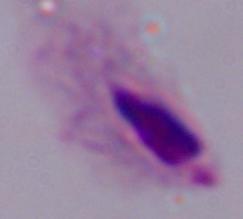 1000x magnification. Photomicrograph. A trichomonad is shown.